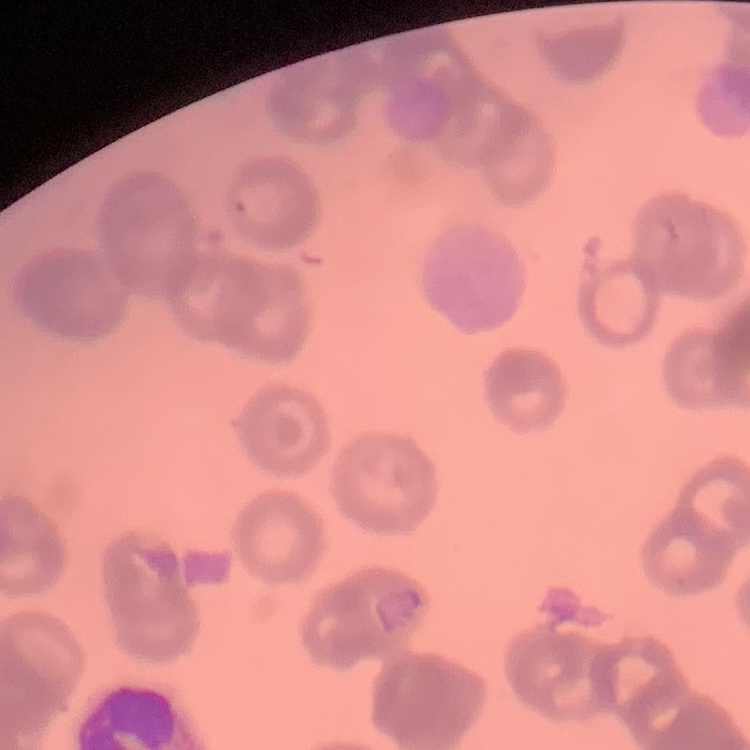
red blood cell morphology = rouleaux formation
preparation = thin peripheral smear
image type = one tile cut from a larger photomicrograph
stain = Field's or Giemsa